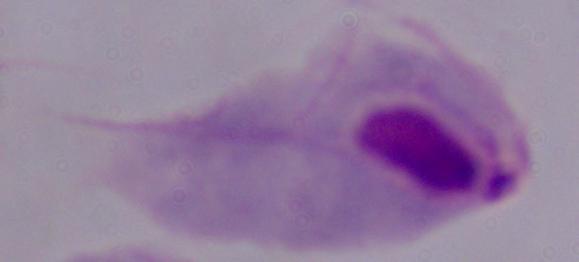

magnification = 1000x
identification = trichomonad
modality = photomicrograph